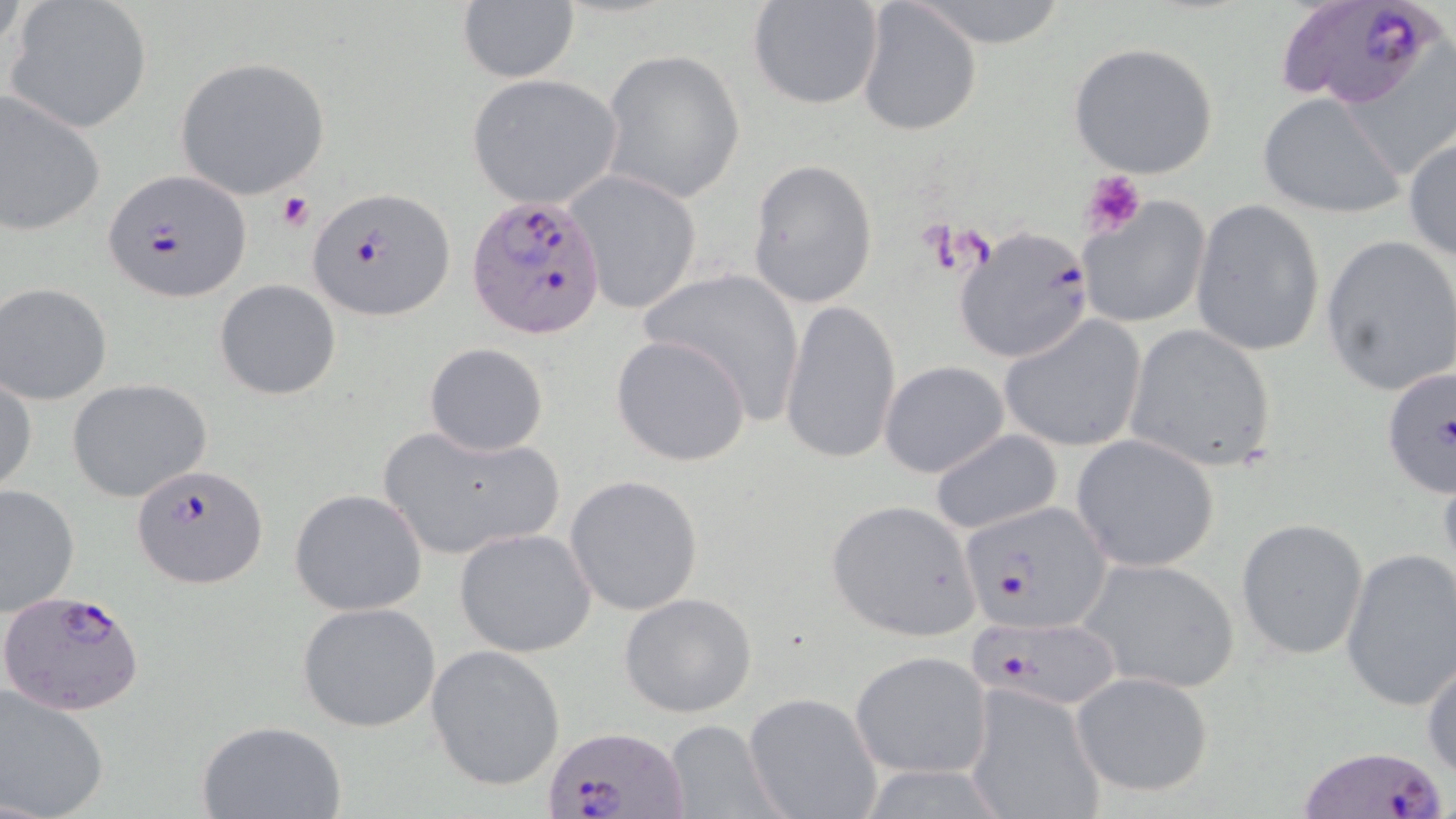
Approximate bounding boxes as [x1, y1, x2, y2] in pixels. Platelet locations: [1081, 168, 1146, 238], [276, 192, 313, 231]. Plasmodium falciparum-infected red blood cell locations: [1278, 1, 1451, 118], [102, 170, 250, 302], [308, 186, 455, 321], [464, 193, 610, 339], [953, 224, 1096, 363], [1378, 365, 1456, 500], [133, 465, 269, 588], [963, 499, 1112, 633], [0, 590, 142, 718], [966, 617, 1122, 707], [540, 724, 687, 819], [1295, 743, 1453, 819]. Uninfected red blood cell locations: [855, 0, 981, 137], [908, 0, 1075, 49], [457, 1, 578, 85], [5, 2, 153, 133], [745, 2, 885, 112], [1068, 41, 1220, 180], [600, 48, 746, 205], [173, 56, 332, 200], [466, 73, 624, 208], [0, 87, 106, 236], [1257, 92, 1404, 219], [1404, 135, 1456, 261], [747, 158, 878, 309], [569, 173, 701, 314], [1078, 198, 1212, 328], [1191, 200, 1324, 356], [1320, 234, 1456, 397], [638, 267, 807, 424], [214, 278, 342, 399], [1, 281, 116, 405], [779, 298, 902, 468], [1000, 314, 1148, 452], [1123, 323, 1279, 473], [610, 334, 752, 467], [423, 343, 548, 456], [879, 360, 1010, 479], [0, 374, 36, 496], [67, 378, 212, 504], [379, 423, 564, 561], [929, 428, 1062, 535], [1072, 435, 1220, 570], [566, 475, 704, 616], [1, 483, 78, 616], [289, 488, 428, 615], [826, 500, 979, 638], [1235, 518, 1369, 659], [454, 528, 596, 657], [1340, 546, 1456, 711], [1075, 556, 1242, 695], [619, 593, 758, 717], [297, 601, 442, 733], [426, 645, 566, 792], [1421, 645, 1455, 781], [849, 651, 992, 780], [1072, 672, 1216, 797], [0, 683, 111, 819], [967, 685, 1105, 819], [743, 692, 881, 819], [195, 720, 348, 819], [661, 720, 786, 819]. Slide-level diagnosis: Plasmodium falciparum. May-Grünwald-Giemsa stain. Captured at 1000x magnification. One field of a larger specimen. Thin blood smear. Image is 1456×819 pixels. Optical microscopy.